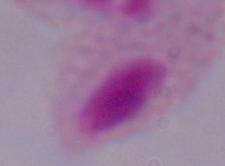

A trichomonad is shown. Micrograph. 1000x magnification.